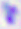 Micrograph. 400x magnification. Toxoplasma gondii is shown.